Classify this cell by malaria status.
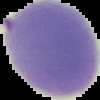

It is uninfected.

Image is 100×100 pixels. From a thin blood smear. The area outside the segmented cell region is set to black.